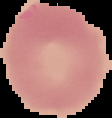

Summary:
  - Image type: cell region segmented out of the field of view; surrounding area masked to black
  - Image size: 112×118 pixels
  - Malaria status: uninfected
  - Preparation: thin blood smear